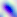 400x magnification. Toxoplasma gondii is seen. Micrograph.